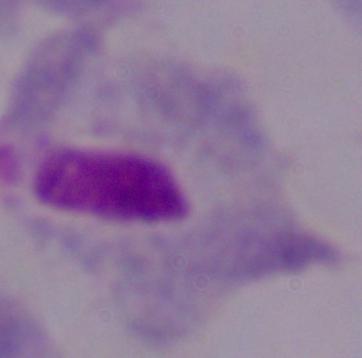
Micrograph. 1000x magnification. A trichomonad is shown.